Comment on the morphology of the erythrocytes.
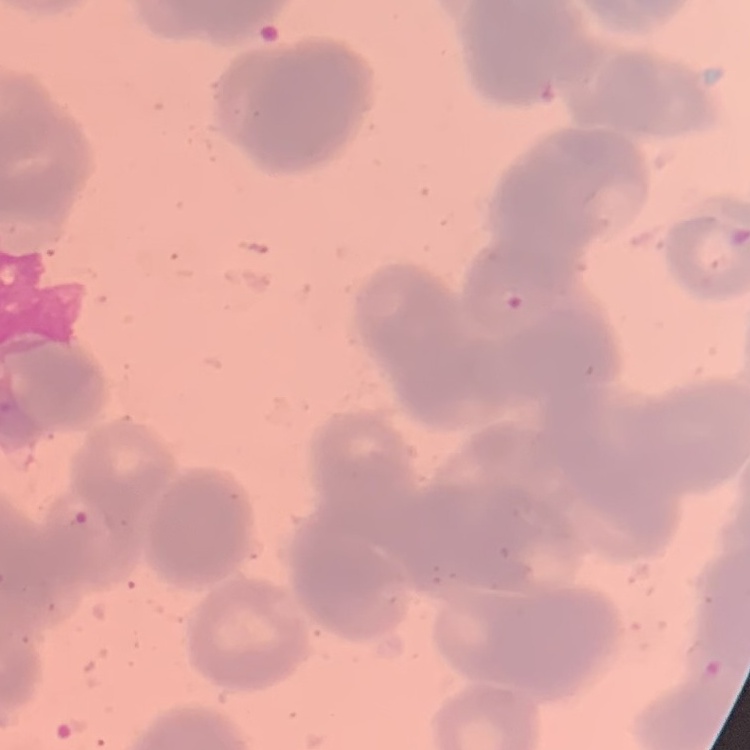

They show rouleaux formation.

{
  "stain": "Field's or Giemsa",
  "image_type": "one tile cut from a larger photomicrograph",
  "preparation": "thin peripheral smear"
}